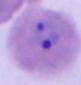
Summary:
  - Identification: Plasmodium
  - Modality: photomicrograph
  - Magnification: 400x or 1000x